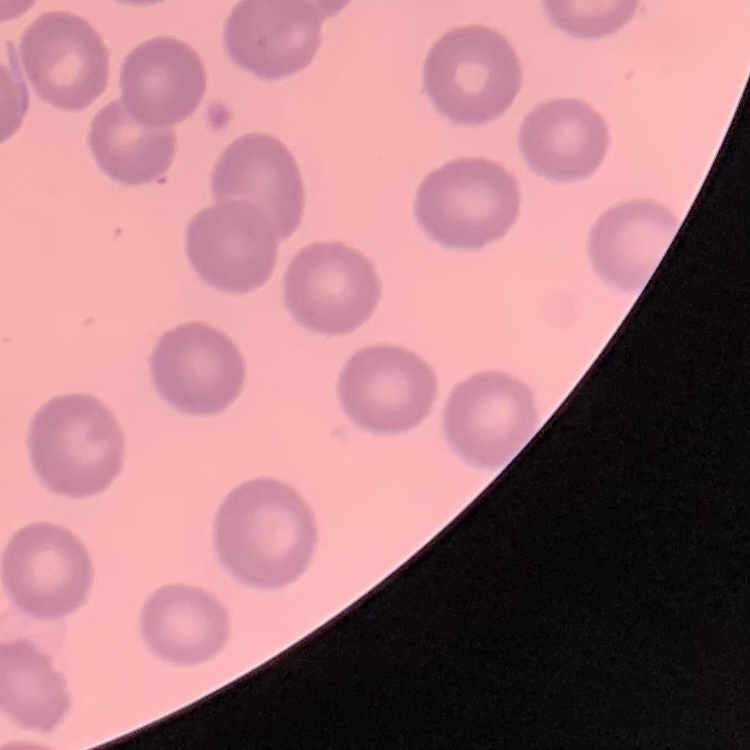

{
  "erythrocyte_morphology": "no rouleaux formation",
  "stain": "Field's or Giemsa",
  "preparation": "thin peripheral smear",
  "image_type": "square crop of a larger photomicrograph"
}